Give the position of every Plasmodium parasite, noting whether each is a trophozoite, schizont, or gametocyte.
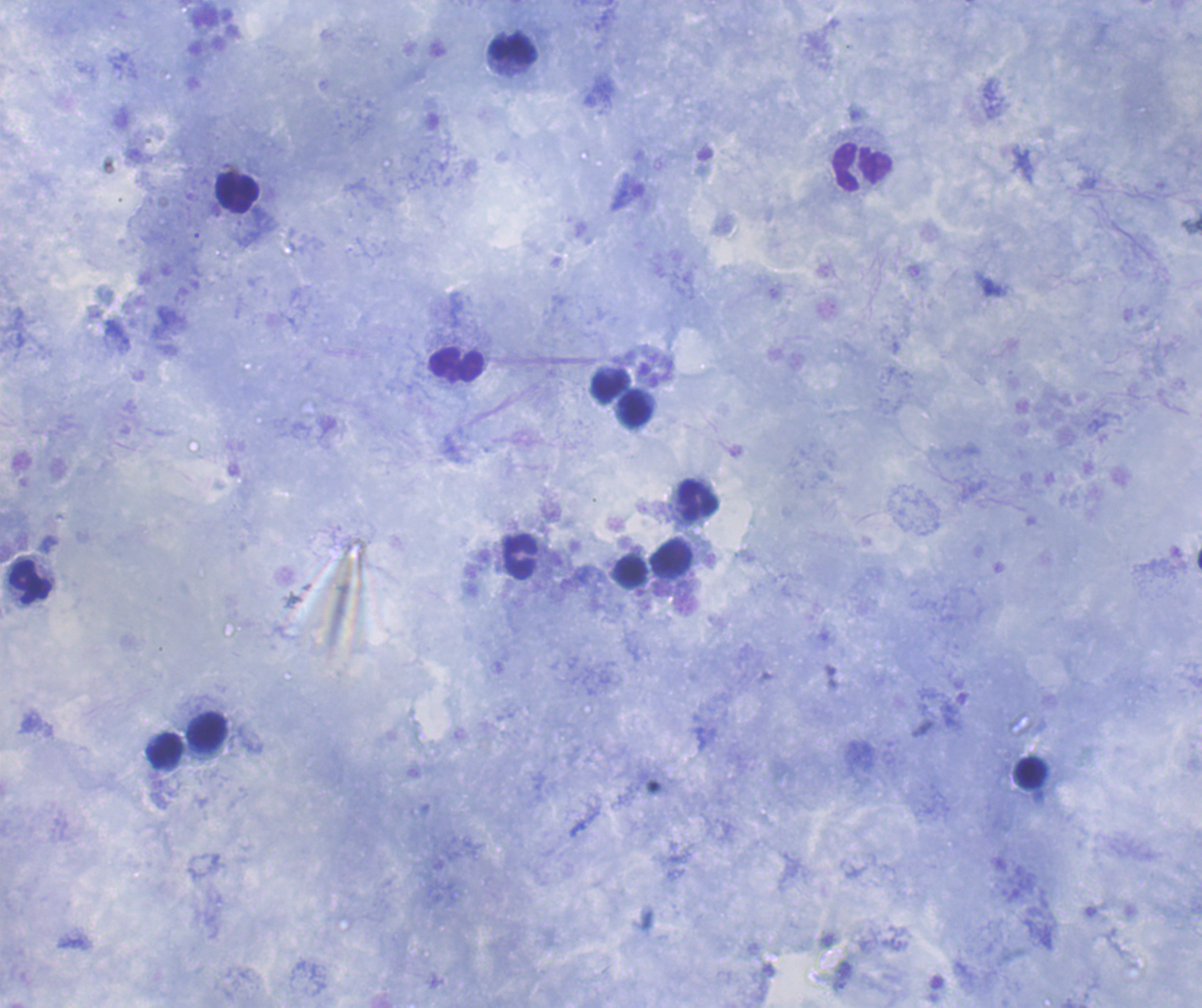
Negative for Plasmodium parasites.

Approximate centers as [x, y] in pixels.
Summary:
  - Leukocyte locations: [512, 49], [862, 167], [237, 193], [456, 365], [610, 385], [634, 410], [697, 500], [520, 556], [672, 558], [631, 571], [30, 582], [207, 731], [165, 750], [1031, 773]
  - Coloration quality: good
  - Preparation: thick blood smear
  - Context: previously used in a real diagnosis
  - Magnification: 100x
  - Image size: 1202×1008 pixels
  - Field of view: one from this slide
  - Stain: Romanowsky
  - Background quality: satisfactory